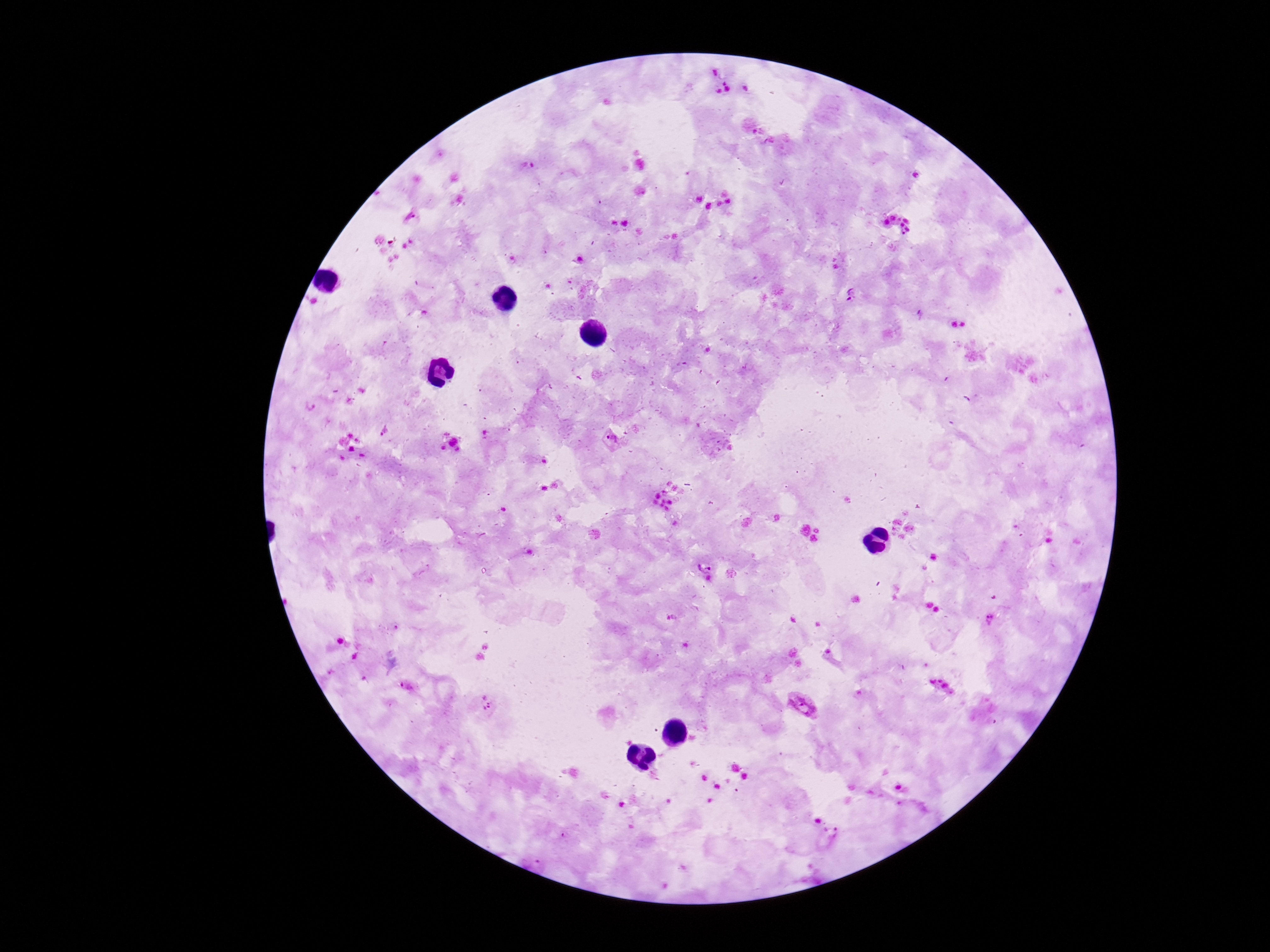

Approximate centers as {x, y} in pixels.
Summary:
  - Plasmodium parasite locations: {524, 168}, {852, 295}, {313, 408}, {613, 440}, {704, 566}, {988, 621}, {408, 687}, {802, 705}, {482, 706}, {830, 833}, {565, 835}, {531, 861}
  - Capture: smartphone camera through the microscope eyepiece
  - Preparation: thick peripheral-blood smear
  - Stain: Giemsa
  - Image size: 1270×952 pixels
  - Patient malaria status: positive
  - Magnification: 100x
  - Field of view: one from this slide